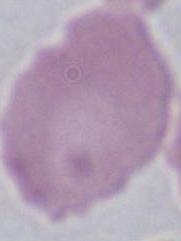
{
  "magnification": "1000x",
  "modality": "micrograph",
  "identification": "erythrocyte"
}